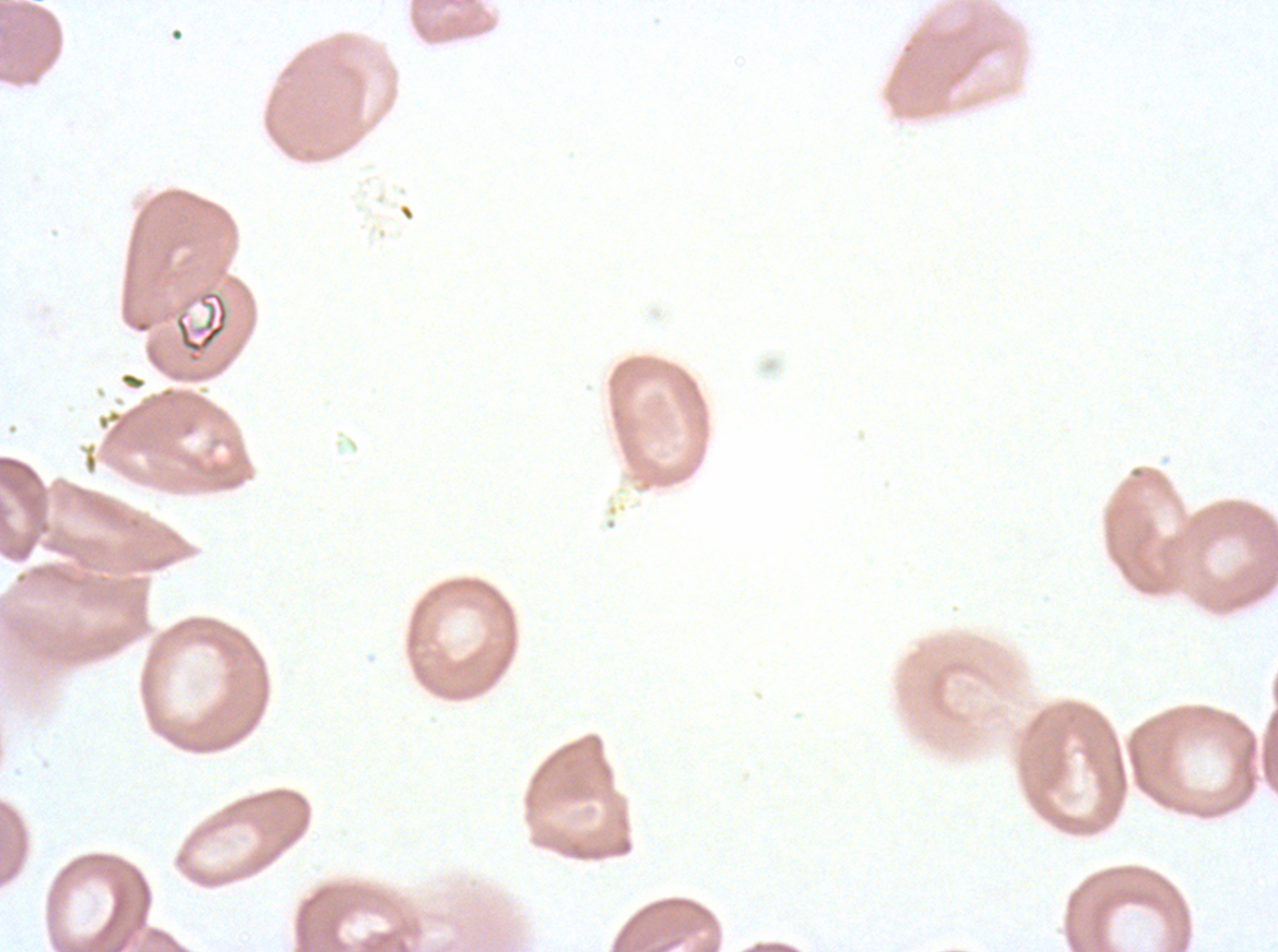

Approximate bounding boxes as {x1, y1, x2, y2} in pixels.
Summary:
  - Debris locations: {173, 289, 229, 364}
  - Field of view: one sub-image of a larger composite
  - Image size: 1278×952 pixels
  - Specimen: Plasmodium falciparum from a patient in The Gambia, cultured ex vivo for 24 to 48 hours
  - Stain: Giemsa
  - Preparation: thin blood film